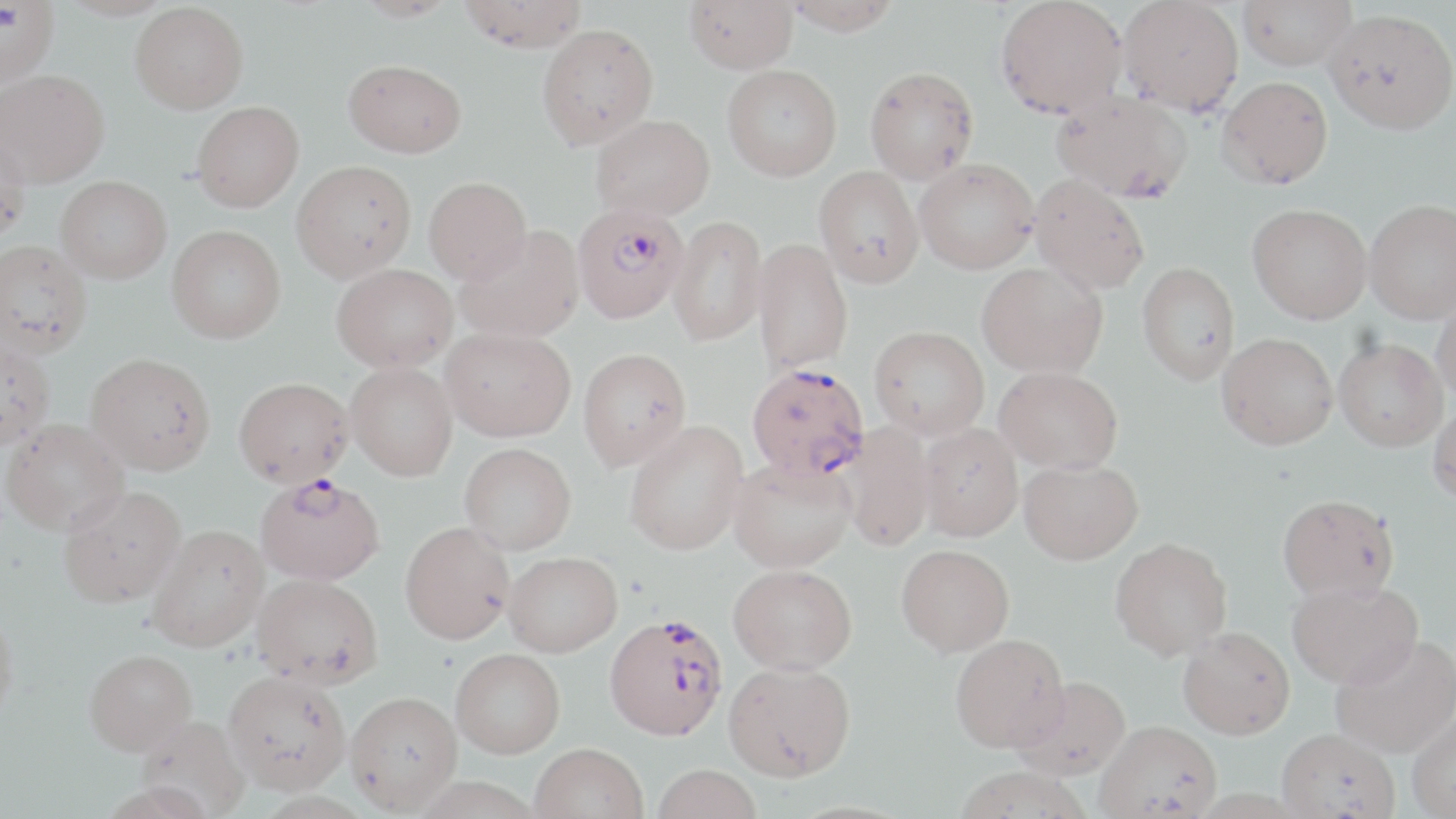 Approximate bounding boxes as (x1, y1, x2, y2) in pixels. Plasmodium falciparum-infected red blood cell locations: (572, 202, 688, 324), (747, 363, 869, 480), (255, 473, 384, 585), (604, 614, 728, 741). Uninfected red blood cell locations: (352, 0, 458, 21), (457, 0, 587, 52), (684, 0, 798, 73), (782, 0, 902, 34), (994, 0, 1129, 119), (1118, 0, 1243, 115), (1238, 0, 1356, 70), (0, 1, 59, 87), (130, 2, 249, 114), (1324, 8, 1456, 135), (536, 24, 658, 149), (343, 59, 467, 158), (722, 64, 842, 181), (864, 66, 979, 184), (0, 69, 109, 187), (1216, 76, 1333, 189), (1051, 90, 1192, 203), (192, 101, 304, 211), (591, 114, 714, 220), (0, 133, 31, 245), (914, 158, 1039, 274), (291, 160, 417, 282), (814, 166, 924, 288), (1029, 173, 1150, 295), (56, 175, 172, 283), (424, 176, 532, 283), (1365, 199, 1456, 323), (1247, 203, 1372, 323), (668, 215, 767, 347), (167, 225, 286, 343), (455, 225, 584, 343), (753, 238, 854, 374), (0, 240, 92, 359), (977, 261, 1107, 377), (1137, 261, 1240, 385), (332, 263, 458, 372), (1432, 296, 1456, 407), (869, 325, 989, 439), (440, 327, 576, 441), (1217, 332, 1338, 449), (1333, 338, 1447, 451), (0, 340, 55, 449), (578, 348, 691, 470), (85, 353, 216, 475), (345, 362, 458, 481), (995, 365, 1123, 474), (233, 377, 354, 488), (1428, 402, 1456, 506), (1, 418, 131, 535), (625, 421, 749, 556), (918, 422, 1023, 541), (840, 424, 934, 552), (459, 442, 576, 554), (728, 458, 856, 573), (1019, 459, 1143, 564), (58, 485, 186, 607), (1277, 493, 1399, 601), (400, 521, 515, 644), (147, 523, 269, 652), (1110, 537, 1233, 660), (896, 544, 1015, 656), (503, 551, 622, 656), (729, 563, 857, 675), (252, 573, 384, 688), (1287, 580, 1422, 688), (0, 609, 19, 727), (1178, 626, 1295, 738), (950, 633, 1069, 752), (1329, 634, 1456, 757), (451, 648, 565, 758), (84, 649, 196, 755), (724, 661, 856, 781), (222, 670, 352, 795), (1011, 676, 1131, 780), (346, 691, 462, 812), (1407, 710, 1456, 818), (135, 715, 250, 818), (1095, 720, 1222, 817), (1277, 727, 1401, 819), (529, 743, 648, 819), (653, 764, 762, 819), (952, 766, 1094, 819). Slide-level diagnosis: Plasmodium falciparum. Single field of view. Image is 1456×819 pixels. May-Grünwald-Giemsa-stained preparation. Captured at 1000x magnification. Light microscopy. Thin blood film.